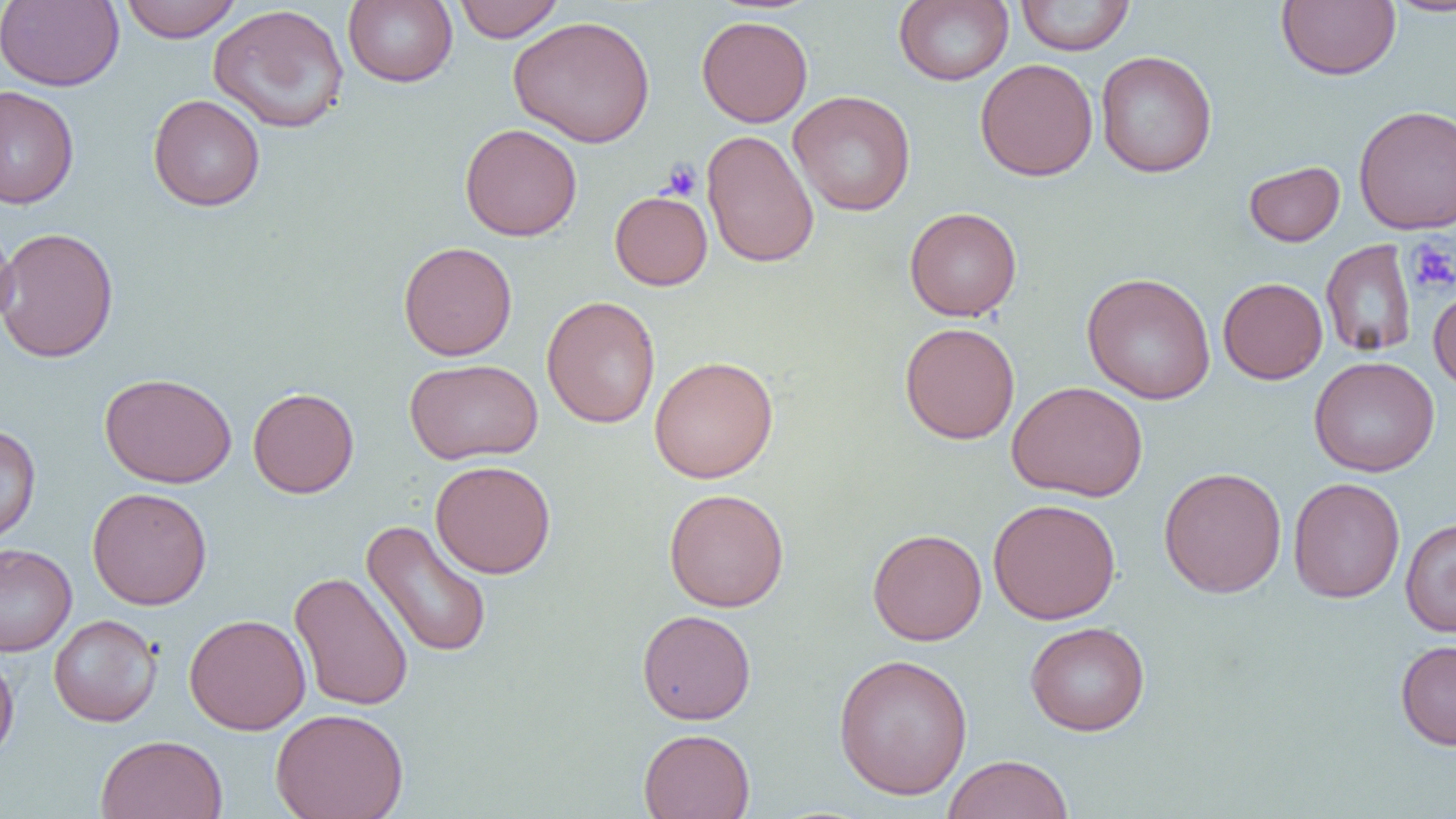
Approximate bounding boxes as [x1, y1, x2, y2] in pixels. Uninfected red blood cell locations: [1, 0, 124, 91], [343, 0, 457, 87], [454, 0, 564, 42], [894, 0, 1014, 86], [1015, 0, 1135, 56], [1276, 0, 1401, 80], [1382, 0, 1456, 17], [120, 1, 242, 43], [207, 4, 349, 134], [508, 14, 656, 148], [696, 15, 813, 127], [1095, 50, 1217, 178], [975, 58, 1098, 181], [0, 85, 80, 210], [788, 91, 916, 216], [148, 94, 265, 212], [1353, 104, 1456, 234], [459, 123, 583, 241], [701, 129, 819, 269], [1243, 160, 1345, 247], [609, 190, 713, 290], [904, 206, 1021, 321], [0, 219, 18, 332], [0, 226, 119, 363], [1320, 240, 1417, 358], [398, 241, 517, 361], [1081, 272, 1217, 405], [1218, 277, 1328, 384], [1428, 284, 1456, 393], [541, 295, 661, 429], [899, 322, 1020, 445], [649, 355, 779, 483], [1308, 356, 1440, 477], [404, 358, 543, 464], [99, 372, 237, 488], [1007, 380, 1148, 502], [248, 386, 360, 498], [0, 423, 41, 547], [430, 460, 556, 578], [1158, 466, 1287, 598], [1287, 477, 1405, 603], [87, 486, 213, 610], [664, 488, 789, 612], [988, 498, 1121, 625], [1400, 517, 1456, 636], [361, 519, 493, 659], [867, 528, 987, 645], [0, 543, 77, 656], [289, 571, 414, 712], [636, 609, 756, 724], [184, 613, 311, 734], [49, 614, 162, 726], [1024, 621, 1151, 736], [1395, 640, 1456, 750], [0, 650, 19, 764], [832, 653, 973, 800], [270, 708, 409, 819], [638, 728, 756, 819], [95, 734, 228, 819], [943, 754, 1074, 819]. Platelet locations: [661, 160, 703, 201], [1406, 237, 1456, 295]. Slide-level diagnosis: negative for blood parasites. Light microscopy. Captured at 1000x magnification. One field of a larger specimen. Thin blood smear. Image is 1456×819 pixels.